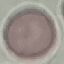

Summary:
  - Malaria status: uninfected
  - Stain: Giemsa
  - Capture: smartphone camera at the microscope eyepiece
  - Image type: cell patch, automatically extracted from a larger field of view and resized to 64 × 64 pixels
  - Preparation: thin blood film